Report the malaria status of this cell.
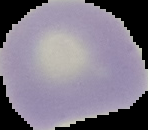

Uninfected.

Segmented cell region on a black background. Image is 148×130 pixels. From a thin blood film.